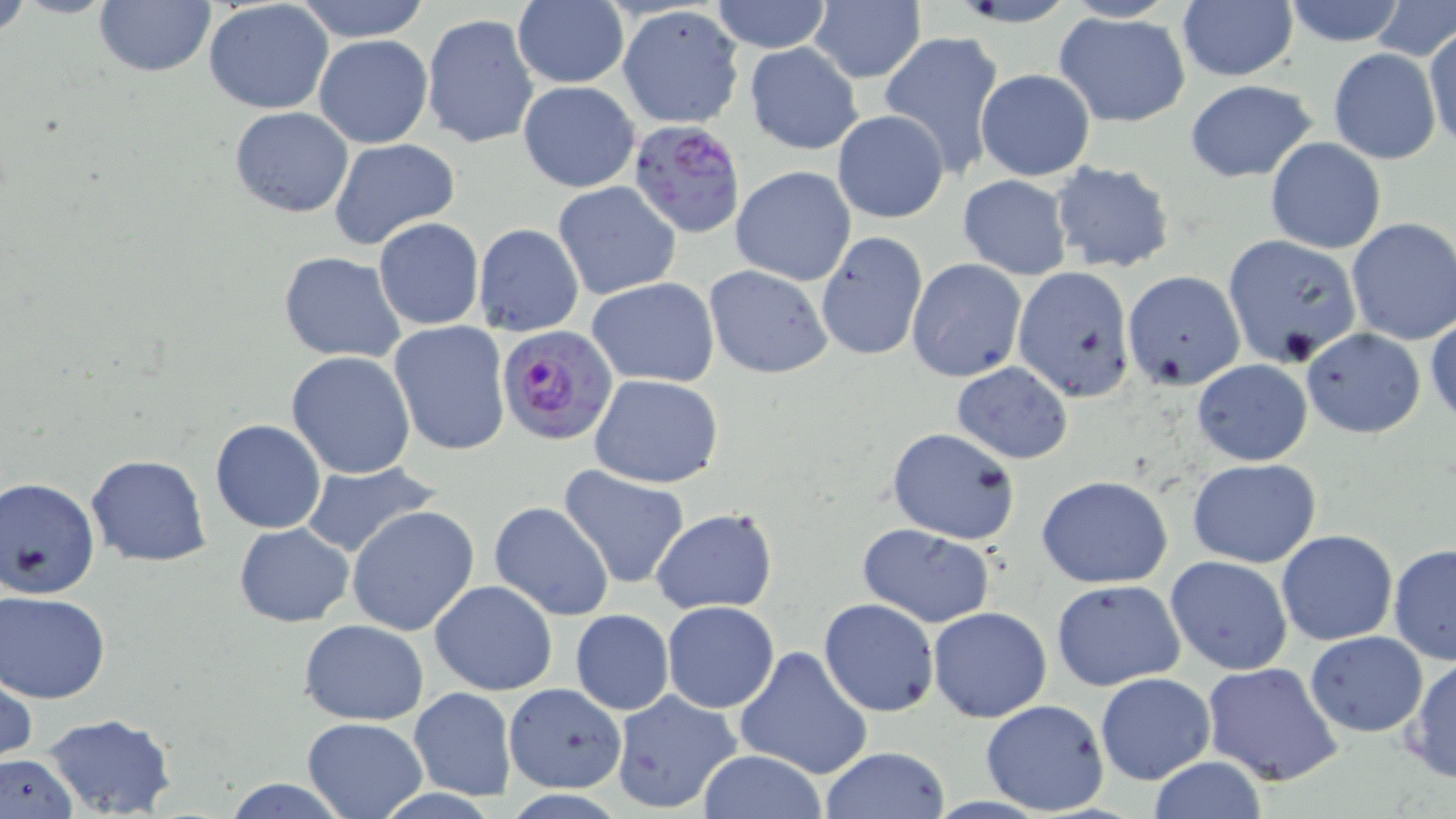
Summary:
  - Coordinate format: approximate bounding boxes as [x1, y1, x2, y2] in pixels
  - Plasmodium falciparum-infected red blood cell locations: [633, 123, 747, 237], [497, 325, 617, 447]
  - Uninfected red blood cell locations: [93, 0, 217, 79], [293, 0, 432, 41], [708, 0, 834, 53], [807, 0, 925, 84], [1279, 0, 1408, 46], [204, 1, 335, 115], [512, 2, 628, 88], [1176, 2, 1297, 83], [616, 5, 744, 129], [1054, 12, 1191, 127], [421, 13, 539, 151], [1423, 26, 1456, 151], [879, 29, 1005, 179], [312, 33, 433, 148], [745, 42, 863, 156], [1328, 48, 1441, 163], [975, 67, 1096, 181], [1183, 79, 1319, 182], [518, 81, 640, 193], [229, 107, 355, 217], [832, 109, 949, 224], [1266, 136, 1386, 253], [329, 138, 461, 250], [1050, 161, 1176, 275], [730, 166, 856, 284], [957, 175, 1074, 279], [553, 181, 681, 301], [374, 217, 485, 330], [1346, 218, 1456, 346], [473, 223, 584, 337], [815, 232, 927, 361], [1222, 233, 1362, 366], [278, 251, 407, 363], [906, 259, 1027, 382], [705, 265, 832, 379], [1012, 266, 1135, 401], [1122, 271, 1246, 390], [587, 276, 720, 387], [388, 322, 510, 454], [1301, 328, 1426, 439], [286, 350, 416, 478], [1192, 358, 1312, 466], [951, 362, 1074, 463], [590, 373, 724, 488], [210, 419, 325, 534], [885, 426, 1020, 545], [87, 454, 211, 567], [1186, 458, 1322, 568], [298, 461, 443, 561], [556, 464, 691, 591], [0, 475, 100, 601], [1037, 475, 1172, 588], [490, 501, 615, 620], [346, 505, 479, 636], [650, 507, 778, 613], [234, 522, 354, 628], [859, 523, 995, 629], [1277, 530, 1398, 645], [1387, 542, 1456, 665], [1166, 555, 1292, 675], [1051, 579, 1185, 691], [429, 580, 558, 695], [1, 590, 111, 704], [819, 597, 939, 717], [662, 601, 779, 713], [929, 605, 1051, 722], [571, 610, 673, 715], [299, 619, 430, 724], [1305, 631, 1428, 737], [733, 646, 874, 781], [1405, 655, 1455, 783], [1, 662, 37, 768], [1202, 662, 1345, 787], [1094, 672, 1216, 785], [502, 682, 626, 791], [410, 688, 516, 799], [609, 689, 743, 814], [979, 698, 1111, 815], [41, 713, 179, 818], [302, 717, 428, 819], [821, 745, 951, 819], [694, 750, 829, 819], [0, 753, 78, 819], [1144, 758, 1272, 818], [221, 778, 351, 817]
  - Slide-level diagnosis: Plasmodium falciparum
  - Field of view: single
  - Stain: May-Grünwald-Giemsa
  - Preparation: thin blood film
  - Modality: light microscopy
  - Image size: 1456×819 pixels
  - Magnification: 1000x